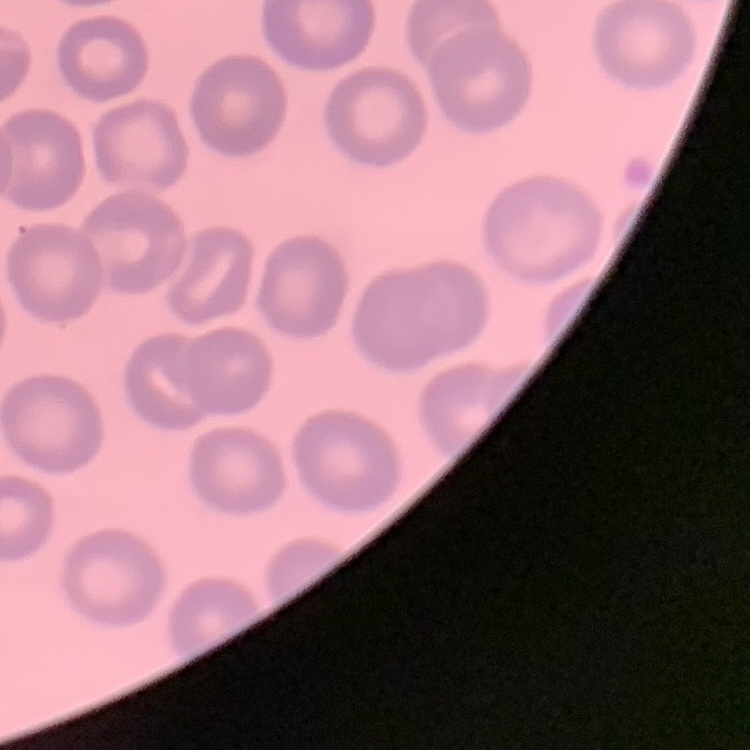

The red blood cells exhibit no rouleaux formation. Thin peripheral smear. Square crop of a larger photomicrograph. Field's or Giemsa stain.